Report the malaria status of this cell.
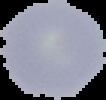
It is uninfected.

Summary:
  - Preparation: thin blood film
  - Image size: 106×100 pixels
  - Image type: segmented cell region with the area outside set to black